Report the malaria status of this cell.
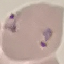
It is parasitized.

preparation = thin blood film
image type = automatically extracted cell patch, resized to 64 × 64 pixels
stain = Giemsa
capture = smartphone through the microscope eyepiece